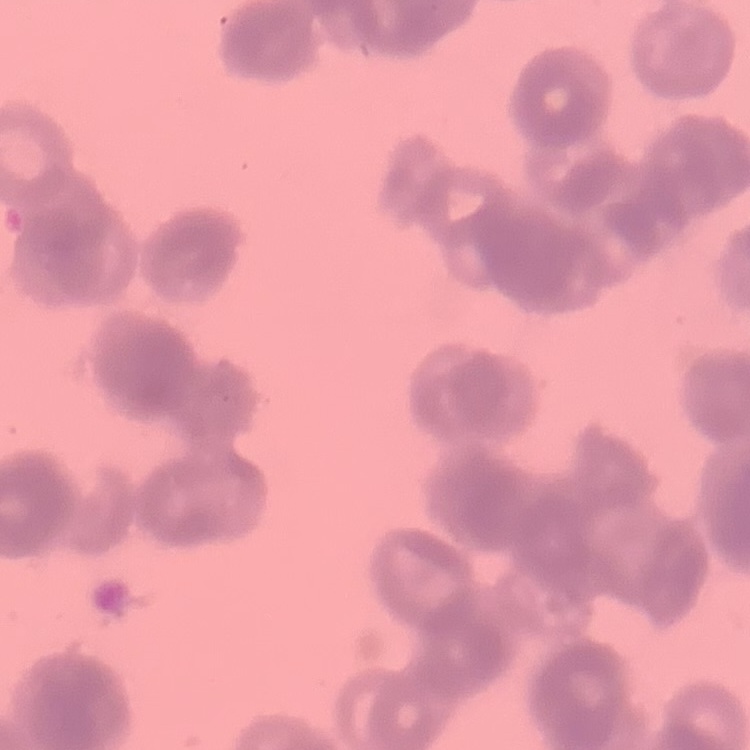

Summary:
  - Red blood cell morphology: rouleaux formation
  - Stain: Field's or Giemsa
  - Image type: one tile cut from a larger photomicrograph
  - Preparation: thin blood film